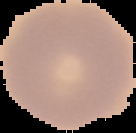

result = no Plasmodium parasites detected
image size = 136×133 pixels
image type = segmented cell region with the area outside set to black
preparation = thin blood smear